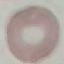

Summary:
  - Result: no malaria parasites seen
  - Capture: smartphone through the microscope eyepiece
  - Image type: cell patch, automatically extracted from a larger field of view and resized to 64 × 64 pixels
  - Preparation: thin blood film
  - Stain: Giemsa